Locate every malaria parasite by life-cycle stage, and every leukocyte.
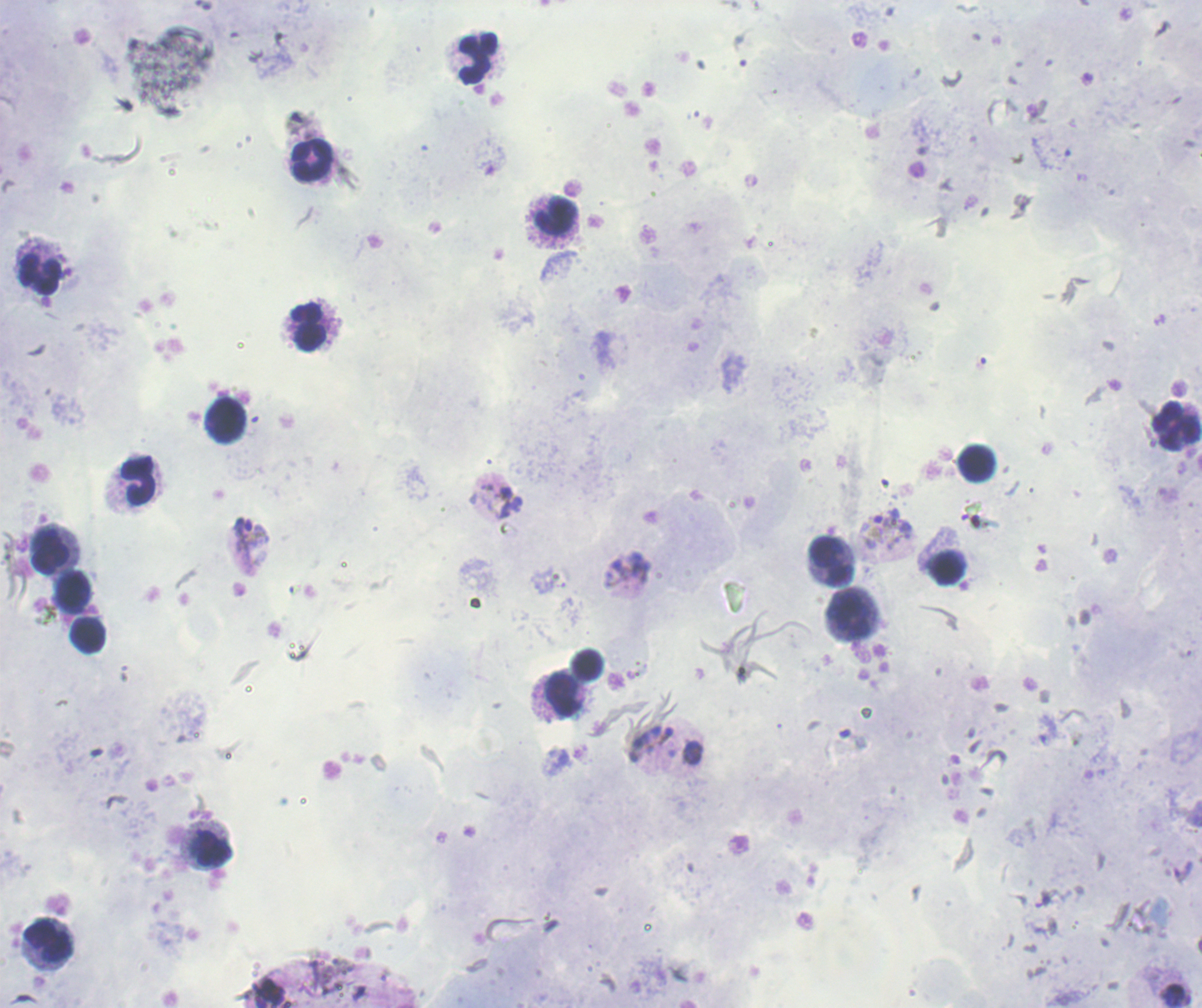

Approximate centers as {x, y} in pixels.
Trophozoites: {981, 364}, {495, 500}, {887, 531}, {628, 570}, {1185, 652}, {1047, 729}, {650, 743}.
Gametocytes: {248, 533}.
No schizont forms observed.
Leukocytes: {478, 58}, {313, 162}, {555, 216}, {41, 275}, {307, 328}, {225, 421}, {1176, 427}, {976, 464}, {137, 480}, {50, 552}, {831, 561}, {947, 568}, {74, 594}, {849, 614}, {88, 636}, {588, 665}, {565, 696}, {210, 848}, {48, 941}.

context: previously used in an actual diagnosis
magnification: 100x
background_quality: good
image_size: 1202×1008 pixels
preparation: thick smear of blood
field_of_view: single
stain: Romanowsky